Assess this cell for malaria.
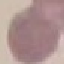
It is uninfected.

preparation = thin blood film
image type = automatically extracted cell patch, resized to 64 × 64 pixels
stain = Giemsa
capture = smartphone camera at the microscope eyepiece